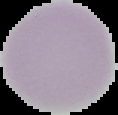

Image is 118×115 pixels. Result: negative for Plasmodium parasites. From a thin blood smear. Cell region segmented out of the field of view; the surrounding area is masked to black.